Comment on the morphology of the erythrocytes.
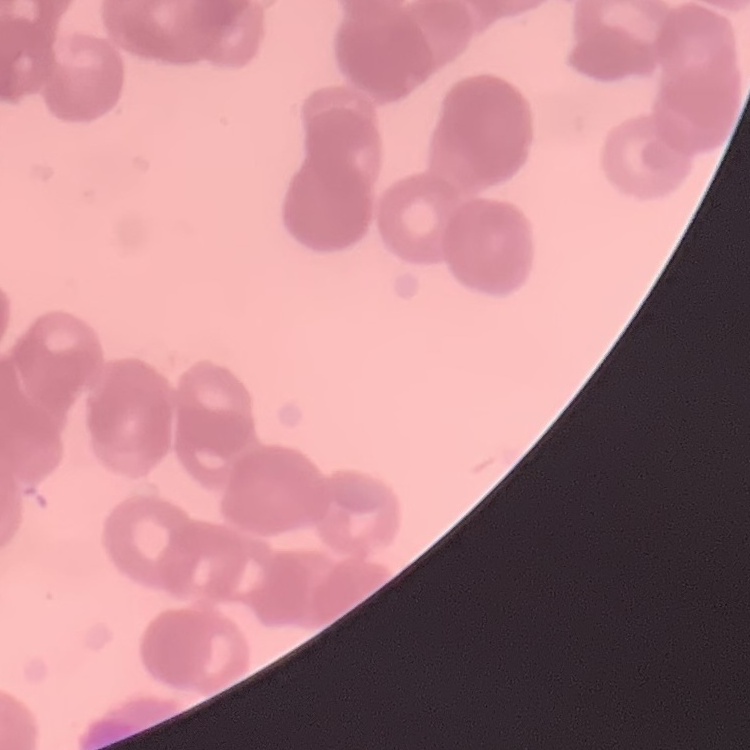

Rouleaux formation.

{
  "stain": "Field's or Giemsa",
  "image_type": "square crop of a larger photomicrograph",
  "preparation": "thin blood film"
}